Assess this cell for malaria.
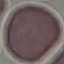

It is uninfected.

image type = automatically extracted cell patch, resized to 64 × 64 pixels
preparation = thin blood film
capture = smartphone camera at the microscope eyepiece
stain = Giemsa